Report the malaria status of this cell.
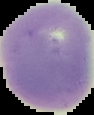

Uninfected.

Image is 94×115 pixels. Cell region segmented out of the field of view; the surrounding area is masked to black. From a thin blood film.